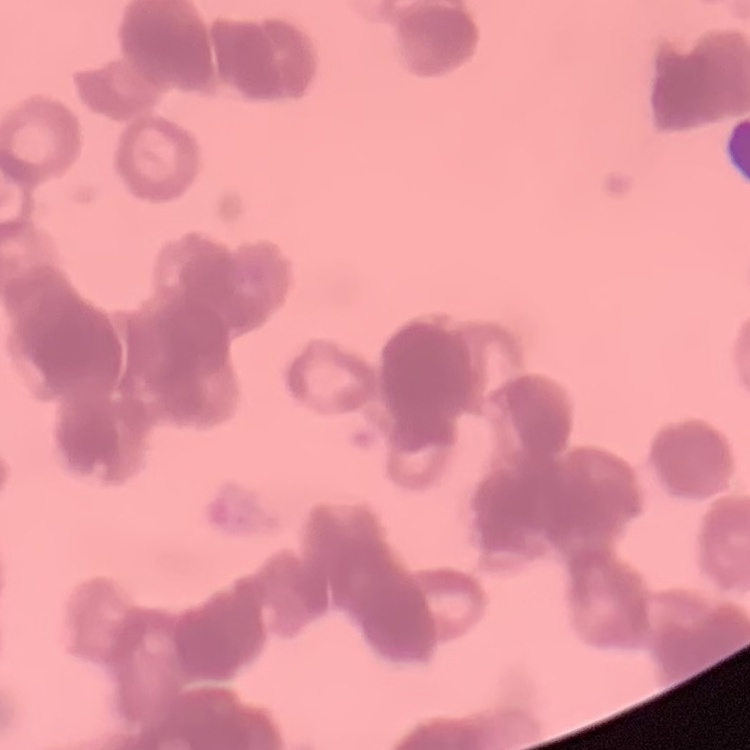

The erythrocytes exhibit rouleaux formation. Thin blood smear. Square crop of a larger photomicrograph. Field's or Giemsa stain.